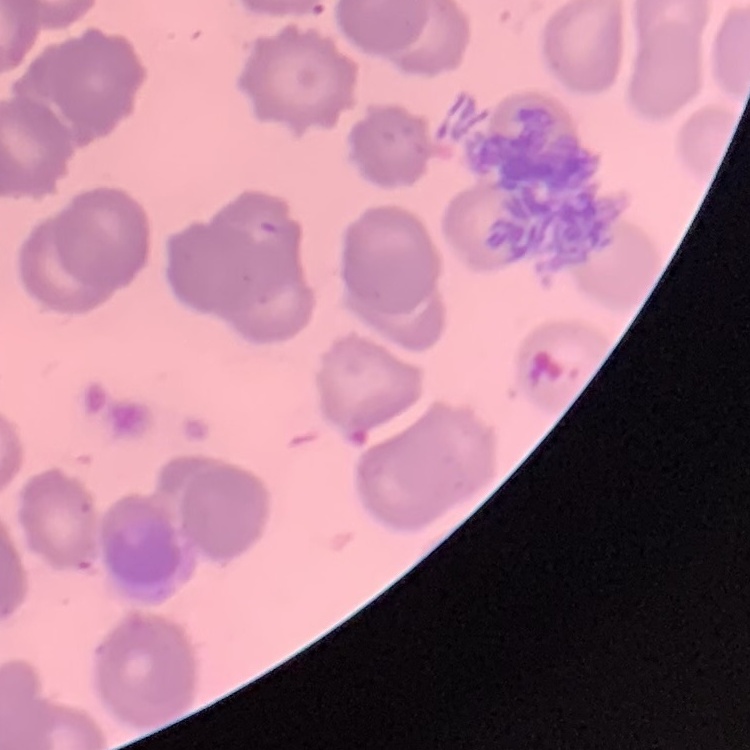
Summary:
  - Red blood cell morphology: rouleaux formation
  - Preparation: thin blood smear
  - Stain: Field's or Giemsa
  - Image type: one tile cut from a larger photomicrograph